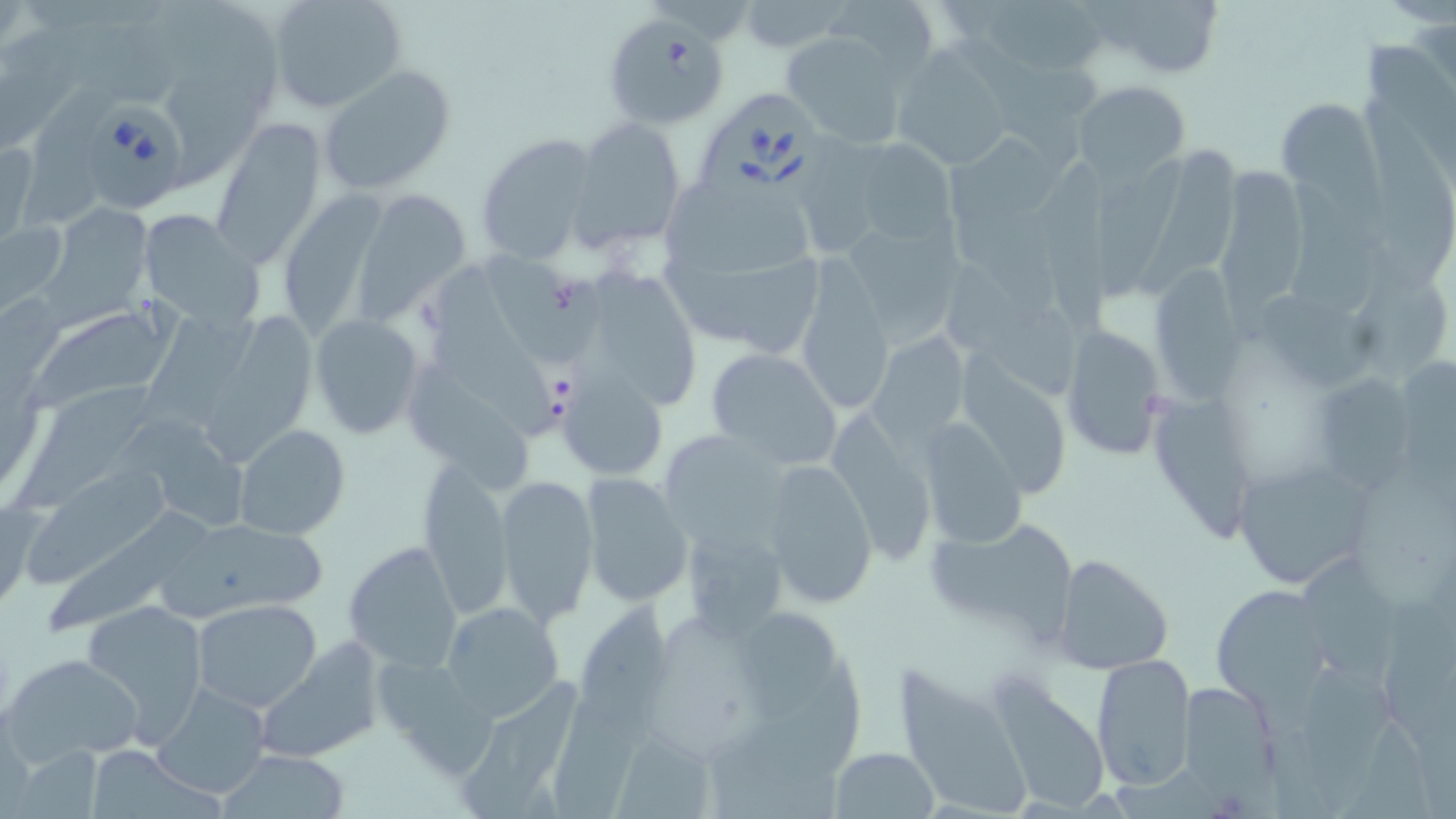
{
  "slide_level_diagnosis": "Babesia divergens",
  "stain": "May-Grünwald-Giemsa",
  "magnification": "1000x",
  "babesia_divergens_infected_red_blood_cell_locations": "approximate bounding boxes as [x1, y1, x2, y2] in pixels: [600, 14, 731, 128], [699, 89, 831, 214], [85, 99, 187, 212]",
  "uninfected_red_blood_cell_locations": "approximate bounding boxes as [x1, y1, x2, y2] in pixels: [169, 0, 283, 106], [266, 0, 408, 114], [969, 0, 1109, 79], [1086, 0, 1229, 81], [825, 1, 940, 75], [738, 2, 847, 52], [76, 18, 195, 104], [0, 20, 97, 152], [780, 28, 913, 149], [959, 37, 1086, 174], [1363, 40, 1456, 190], [893, 49, 1014, 170], [319, 65, 456, 195], [171, 68, 275, 191], [1074, 80, 1190, 181], [24, 83, 104, 231], [1278, 98, 1383, 204], [1368, 101, 1456, 285], [570, 116, 688, 251], [211, 122, 325, 268], [802, 131, 886, 249], [475, 132, 599, 266], [946, 135, 1061, 217], [851, 139, 960, 252], [0, 142, 40, 246], [1138, 147, 1242, 297], [1100, 153, 1195, 305], [1039, 159, 1121, 344], [1213, 166, 1309, 313], [661, 181, 812, 286], [1288, 182, 1383, 316], [356, 187, 473, 318], [277, 193, 387, 339], [46, 203, 154, 319], [956, 207, 1061, 318], [138, 209, 265, 328], [833, 211, 966, 348], [1, 218, 68, 315], [662, 249, 830, 351], [1349, 250, 1450, 380], [482, 255, 600, 366], [938, 256, 1082, 403], [793, 258, 895, 419], [590, 261, 696, 410], [422, 263, 555, 439], [1153, 265, 1254, 410], [1267, 293, 1378, 391], [23, 298, 190, 411], [143, 305, 265, 428], [214, 311, 321, 466], [308, 314, 425, 439], [1056, 324, 1169, 460], [867, 331, 973, 448], [705, 346, 844, 470], [1407, 357, 1456, 514], [409, 362, 534, 495], [556, 371, 668, 481], [1315, 376, 1414, 501], [14, 380, 160, 512], [1155, 398, 1255, 545], [833, 413, 939, 561], [121, 415, 250, 531], [914, 419, 1029, 550], [233, 423, 351, 539], [668, 432, 792, 551], [758, 456, 881, 608], [1230, 456, 1374, 589], [29, 462, 182, 584], [415, 465, 513, 618], [496, 474, 598, 626], [581, 474, 693, 608], [1, 495, 42, 612], [50, 512, 212, 635], [923, 516, 1079, 641], [181, 518, 331, 613], [679, 522, 794, 639], [344, 540, 463, 671], [1053, 554, 1174, 676], [1305, 560, 1398, 688], [1211, 583, 1330, 708], [578, 598, 670, 752], [80, 600, 210, 737], [193, 600, 323, 714], [440, 601, 564, 723], [735, 607, 838, 724], [252, 648, 382, 762], [4, 652, 144, 763], [370, 652, 493, 769], [1090, 653, 1197, 791], [731, 654, 866, 779], [892, 659, 1034, 817], [1301, 668, 1397, 801], [458, 673, 582, 819], [1179, 681, 1279, 799], [151, 683, 271, 800], [990, 685, 1108, 811], [548, 701, 646, 819], [1334, 723, 1434, 819], [616, 734, 716, 819], [9, 744, 103, 819], [82, 745, 218, 818], [711, 747, 836, 819], [830, 747, 939, 818], [216, 749, 352, 818]",
  "field_of_view": "single",
  "preparation": "thin blood film",
  "image_size": "1456×819 pixels",
  "modality": "light microscopy"
}